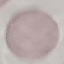
Summary:
  - Result: no malaria parasites seen
  - Capture: smartphone through the microscope eyepiece
  - Stain: Giemsa
  - Preparation: thin smear
  - Image type: automatically extracted cell patch, resized to 64 × 64 pixels